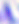

modality = micrograph
magnification = 400x
identification = Toxoplasma gondii